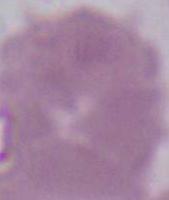
1000x magnification. A red blood cell is shown. Micrograph.